State which parasite is depicted.
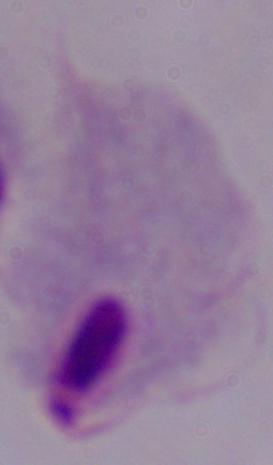
A trichomonad.

modality = micrograph
magnification = 1000x